State which parasite is depicted.
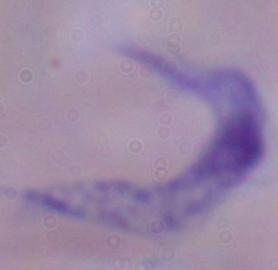
This is a trypanosome.

Micrograph. Captured at 1000x magnification.